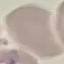
result = no malaria parasites detected
preparation = thin blood film
stain = Giemsa
image type = automatically extracted cell patch, resized to 64 × 64 pixels
capture = smartphone camera at the microscope eyepiece